Give the preparation type.
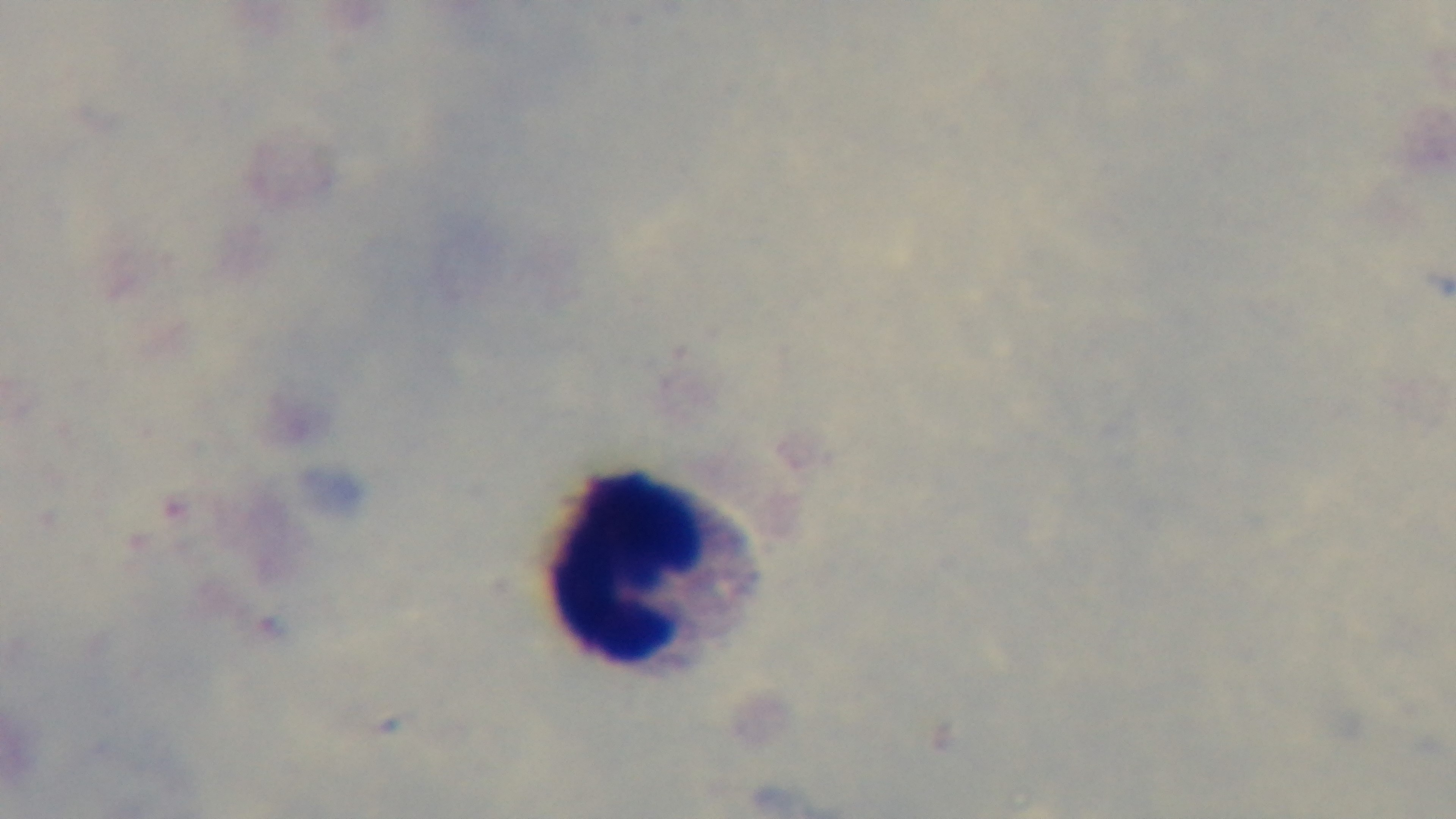

Thick.

Malaria status: negative. One field from the slide. 100x oil-immersion objective. Light microscopy. Giemsa-stained. Captured with a mounted 4K digital camera.